Report the malaria status of this cell.
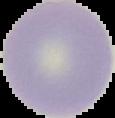

Uninfected.

Summary:
  - Image size: 115×118 pixels
  - Preparation: thin blood smear
  - Image type: segmented cell region with the area outside set to black